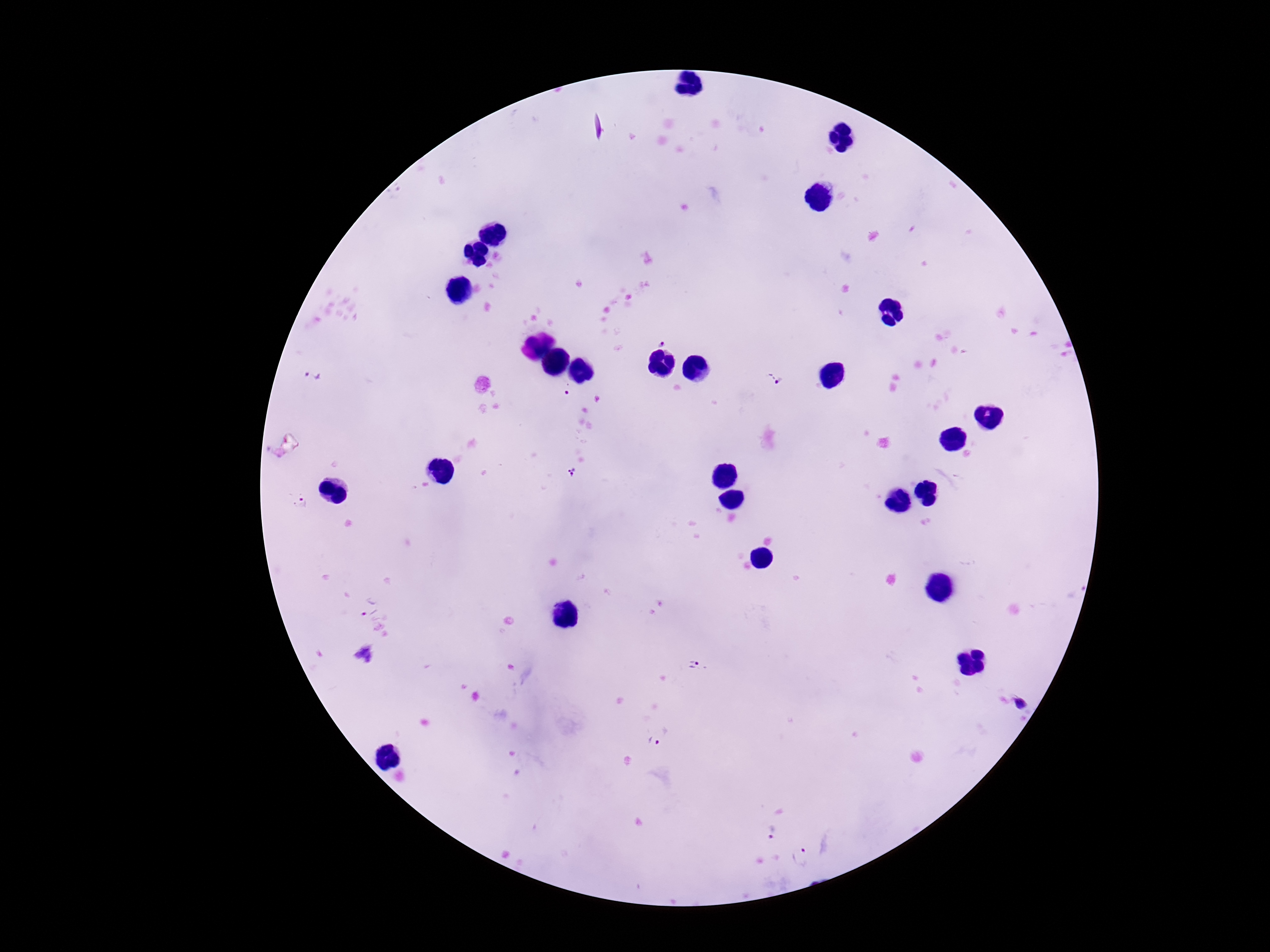

Approximate centers as (x, y) in pixels. Plasmodium parasite locations: (660, 340), (773, 377), (315, 379), (567, 390), (571, 471), (368, 606), (695, 667), (1021, 705), (654, 741), (771, 832), (802, 855). Photographed through the microscope eyepiece with a smartphone camera. One field from this slide. Patient malaria status: positive. Giemsa stain. 100x magnification. Image is 1270×952 pixels. Thick blood film.